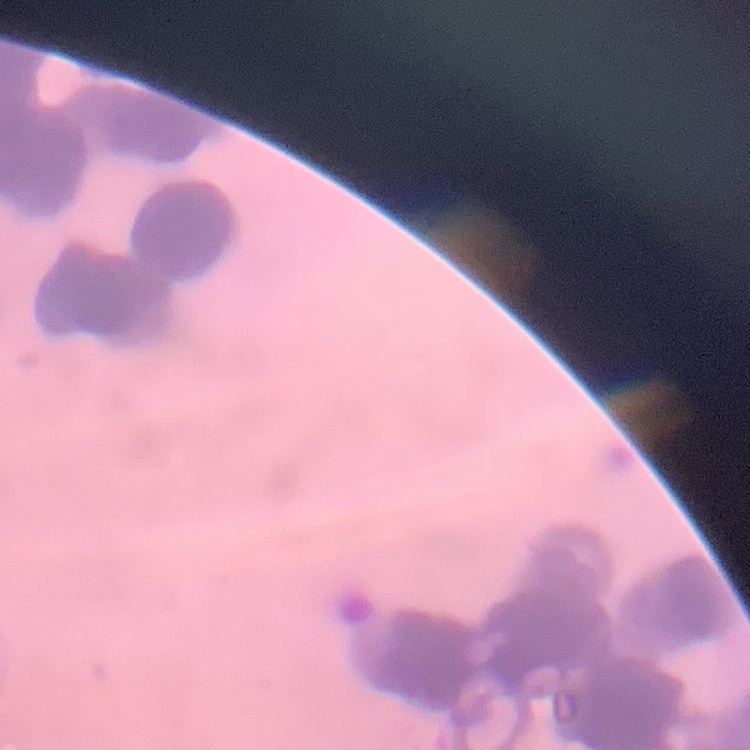
Summary:
  - Erythrocyte morphology: rouleaux formation
  - Preparation: thin blood smear
  - Image type: square crop of a larger photomicrograph
  - Stain: Field's or Giemsa